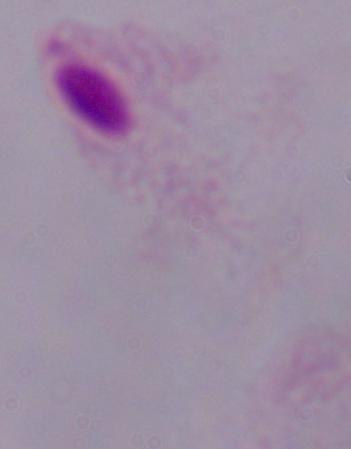
A trichomonad is seen. Micrograph. 1000x magnification.